Identify the parasite.
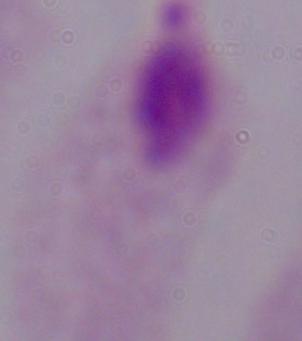
This is a trichomonad.

modality = micrograph
magnification = 1000x